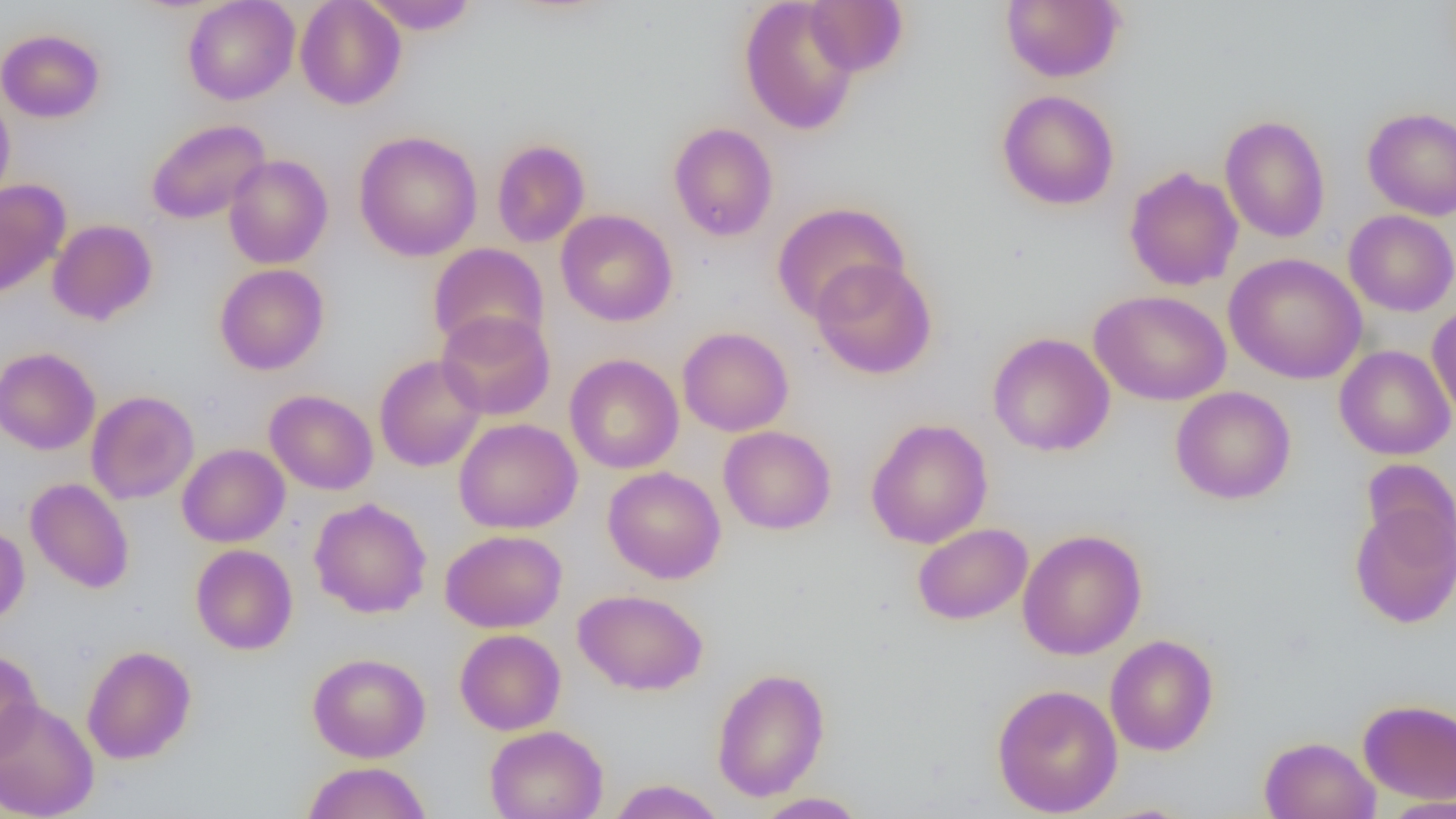

slide-level diagnosis = no evidence of blood parasites
magnification = 1000x
modality = optical microscopy
preparation = thin blood film
field of view = one of a larger specimen
image size = 1456×819 pixels
uninfected red blood cell locations = approximate bounding boxes as [x1, y1, x2, y2] in pixels: [183, 0, 300, 105], [295, 0, 407, 110], [362, 0, 478, 35], [739, 0, 861, 135], [803, 0, 909, 77], [1001, 0, 1124, 83], [0, 28, 105, 123], [0, 89, 15, 205], [997, 89, 1120, 211], [1362, 106, 1456, 220], [1220, 115, 1331, 243], [146, 119, 270, 224], [668, 122, 778, 242], [354, 130, 483, 262], [492, 139, 590, 248], [223, 155, 333, 269], [1124, 166, 1243, 291], [0, 179, 70, 300], [771, 201, 909, 322], [556, 209, 677, 327], [1343, 210, 1456, 316], [47, 219, 158, 325], [428, 242, 549, 354], [1224, 252, 1367, 385], [811, 259, 937, 379], [214, 263, 329, 375], [1090, 289, 1231, 406], [1427, 305, 1456, 423], [436, 310, 556, 420], [677, 327, 794, 436], [988, 332, 1115, 456], [1334, 345, 1455, 461], [0, 347, 101, 455], [564, 354, 684, 474], [374, 355, 487, 472], [1170, 386, 1296, 504], [265, 389, 378, 495], [86, 390, 199, 505], [454, 417, 583, 534], [865, 418, 993, 549], [718, 425, 837, 535], [177, 443, 289, 547], [1360, 458, 1456, 567], [602, 466, 726, 583], [26, 477, 134, 593], [309, 497, 432, 618], [1349, 499, 1456, 629], [0, 523, 29, 626], [913, 523, 1033, 625], [440, 529, 568, 633], [1017, 529, 1146, 660], [190, 544, 298, 654], [573, 588, 709, 696], [454, 628, 566, 735], [1105, 634, 1218, 755], [81, 645, 196, 764], [0, 648, 43, 763], [307, 652, 431, 763], [711, 666, 830, 802], [991, 683, 1123, 817], [0, 698, 100, 819], [1358, 698, 1456, 804], [484, 725, 609, 819], [1259, 736, 1381, 819], [301, 761, 433, 819], [606, 778, 727, 819], [752, 792, 868, 818], [1381, 796, 1456, 818]